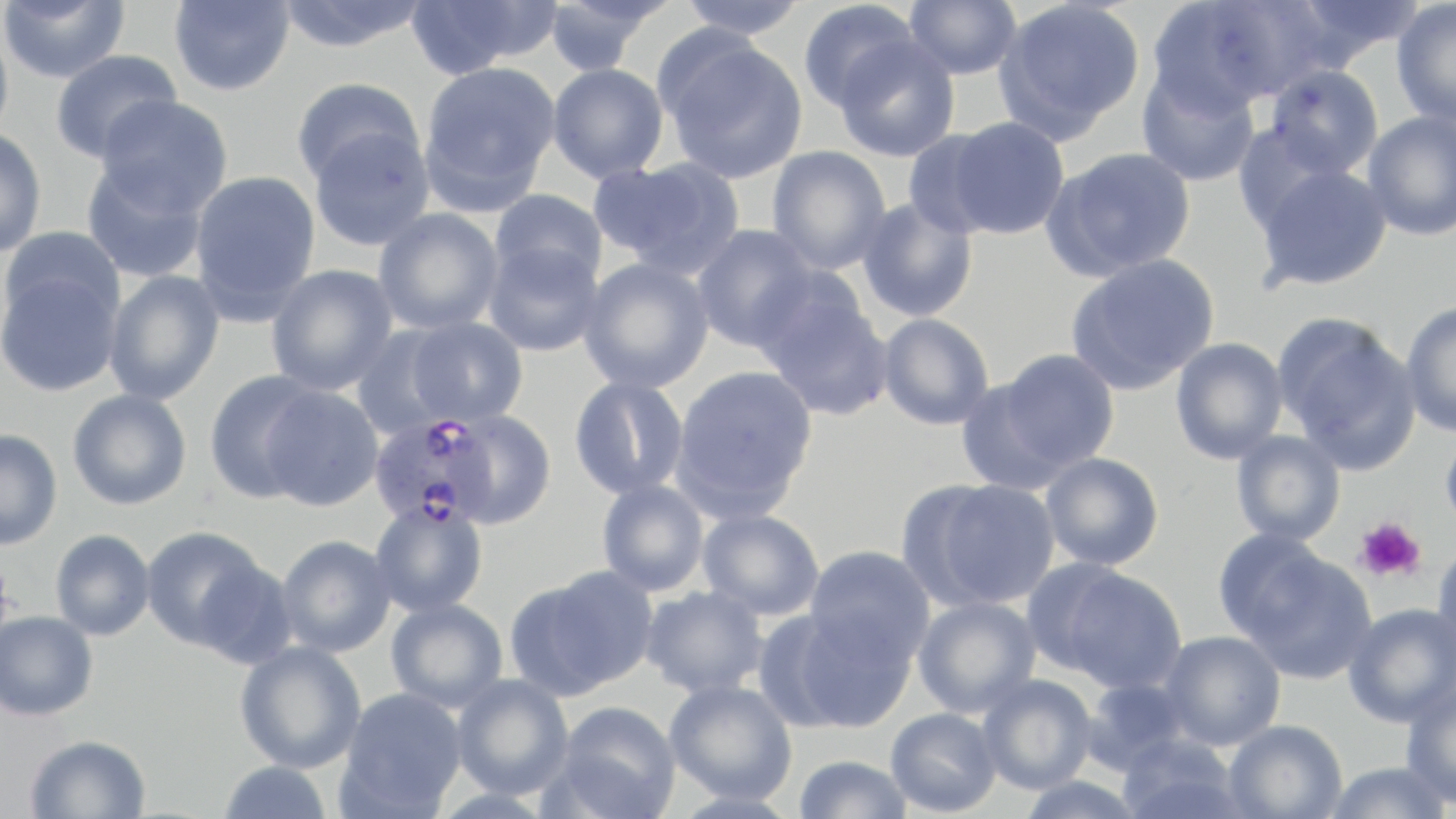
Summary:
  - Coordinate format: approximate bounding boxes as (x1, y1, x2, y2) in pixels
  - Uninfected red blood cell locations: (0, 0, 130, 84), (169, 0, 295, 97), (275, 0, 431, 52), (405, 0, 560, 76), (543, 0, 672, 75), (676, 0, 810, 40), (797, 0, 922, 112), (904, 0, 1022, 80), (1148, 0, 1307, 116), (1287, 0, 1429, 66), (993, 1, 1146, 143), (1391, 1, 1456, 131), (0, 20, 14, 147), (659, 36, 808, 184), (833, 36, 961, 162), (49, 49, 181, 163), (419, 61, 560, 212), (547, 63, 669, 183), (1264, 64, 1385, 179), (1135, 67, 1261, 188), (292, 77, 426, 186), (96, 95, 232, 218), (1362, 111, 1456, 241), (940, 116, 1070, 239), (0, 127, 48, 257), (308, 127, 435, 252), (901, 129, 1007, 239), (766, 145, 891, 275), (1042, 147, 1196, 281), (590, 156, 745, 280), (81, 162, 209, 283), (1252, 162, 1393, 292), (189, 170, 321, 321), (489, 189, 608, 290), (857, 196, 979, 323), (373, 208, 503, 335), (692, 224, 818, 352), (1, 227, 124, 333), (483, 242, 604, 356), (1065, 254, 1220, 395), (578, 257, 715, 394), (266, 264, 398, 396), (0, 266, 123, 397), (103, 270, 224, 406), (760, 292, 895, 422), (1400, 301, 1456, 438), (877, 312, 995, 430), (1274, 313, 1421, 473), (401, 316, 528, 429), (350, 324, 463, 440), (1170, 337, 1288, 465), (994, 349, 1120, 473), (670, 365, 819, 520), (204, 370, 327, 502), (568, 375, 690, 500), (954, 377, 1078, 496), (258, 385, 384, 511), (67, 389, 192, 510), (443, 409, 558, 528), (1440, 426, 1456, 536), (0, 429, 63, 550), (1230, 430, 1346, 547), (1040, 452, 1165, 571), (907, 478, 1061, 611), (596, 479, 710, 597), (369, 500, 489, 617), (697, 508, 825, 621), (140, 526, 269, 650), (1211, 528, 1336, 646), (50, 529, 156, 641), (276, 534, 396, 657), (1431, 542, 1456, 665), (804, 545, 936, 668), (1230, 547, 1377, 684), (193, 559, 299, 671), (1047, 566, 1188, 694), (509, 568, 655, 699), (641, 586, 768, 698), (913, 595, 1042, 718), (385, 598, 508, 713), (1343, 603, 1456, 728), (781, 608, 918, 732), (0, 610, 99, 720), (1160, 631, 1286, 750), (234, 640, 367, 773), (451, 674, 574, 799), (977, 674, 1097, 795), (1079, 677, 1193, 774), (664, 680, 798, 805), (1400, 683, 1456, 809), (339, 687, 467, 815), (552, 701, 682, 819), (885, 707, 1002, 816), (1223, 720, 1348, 818), (25, 734, 151, 819), (1116, 735, 1247, 819), (793, 754, 913, 818), (218, 760, 332, 819), (1322, 761, 1452, 819), (1015, 775, 1148, 819)
  - Platelet locations: (1353, 517, 1427, 583)
  - Plasmodium falciparum-infected red blood cell locations: (368, 413, 497, 530)
  - Slide-level diagnosis: Plasmodium falciparum
  - Magnification: 1000x
  - Preparation: thin blood film
  - Modality: light microscopy
  - Image size: 1456×819 pixels
  - Stain: May-Grünwald-Giemsa
  - Field of view: single